Point out every malaria parasite and every leukocyte.
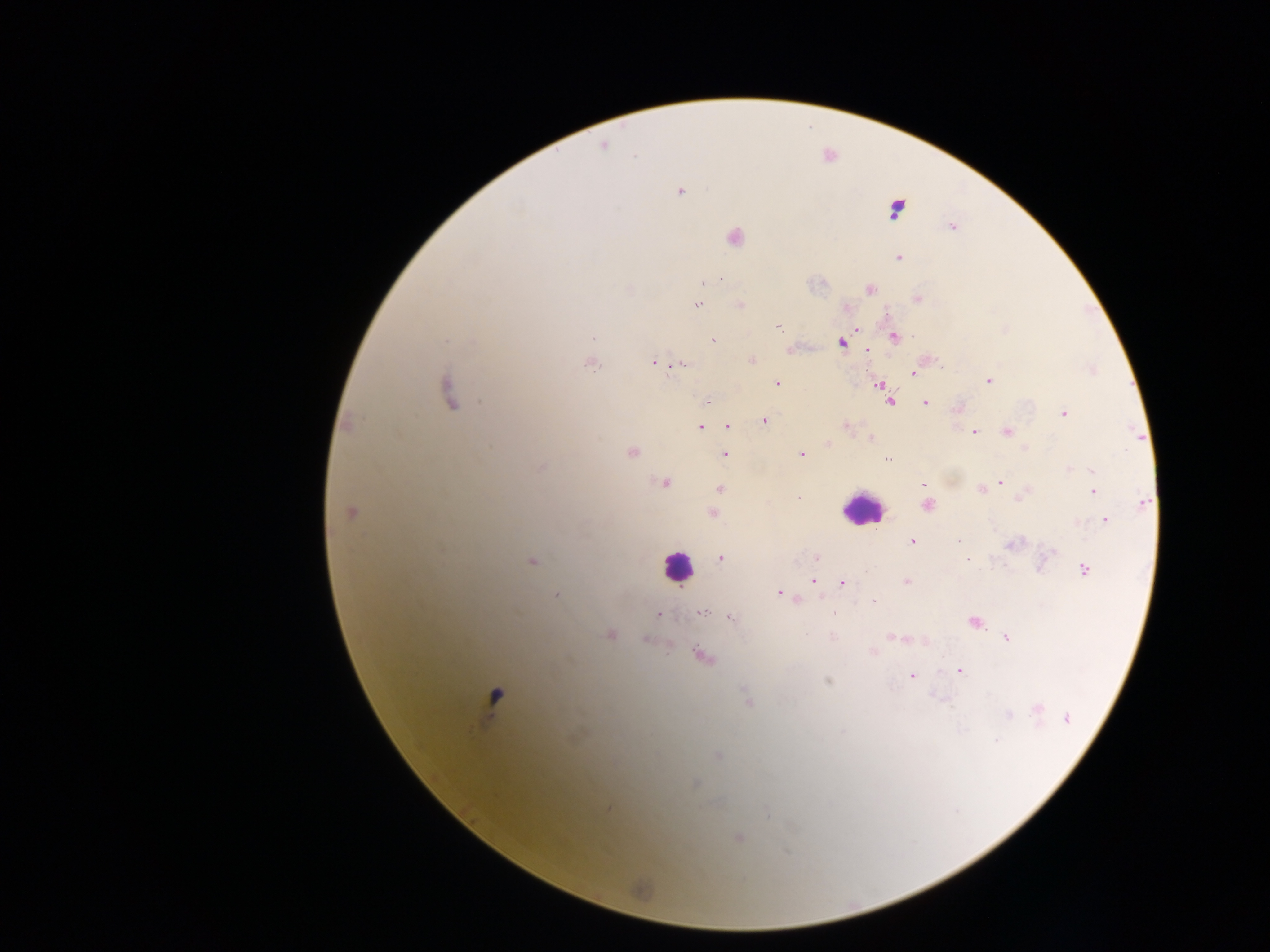
Approximate centers as (x, y) in pixels.
Malaria parasites: (604, 147), (678, 191), (895, 209), (952, 226), (734, 236), (899, 257), (715, 279), (720, 279), (703, 281), (870, 288), (917, 298), (697, 305), (740, 305), (846, 307), (778, 328), (854, 328), (593, 335), (894, 335), (713, 340), (841, 342), (789, 350), (868, 351), (751, 360), (653, 361), (590, 362), (679, 364), (913, 373), (988, 380), (777, 383), (879, 385), (447, 390), (889, 400), (924, 402), (957, 408), (1063, 414), (764, 421), (845, 424), (728, 425), (700, 426), (1007, 431), (973, 432), (870, 438), (827, 443), (631, 451), (724, 454), (801, 454), (888, 458), (541, 467), (1093, 470), (664, 482), (1000, 482), (924, 485), (719, 488), (981, 488), (1092, 490), (1025, 494), (1141, 503), (927, 505), (350, 511), (711, 513), (1105, 519), (911, 541), (1012, 544), (720, 557), (815, 557), (532, 560), (1084, 570), (812, 581), (905, 581), (842, 582), (779, 592), (556, 595), (796, 599), (700, 612), (658, 614), (729, 616), (974, 621), (608, 634), (831, 636), (896, 637), (1006, 637), (644, 640), (872, 652), (700, 655), (959, 670), (910, 676), (828, 680), (495, 696), (748, 702), (1037, 708), (1008, 715), (1067, 717), (995, 740), (717, 755), (693, 784), (608, 808), (739, 837).
Leukocytes: (863, 509), (677, 566).

Image is 1270×952 pixels. Collected in Ghana. Single field of view. Mobile-phone photograph taken through the microscope. Thick blood smear.